Assess the morphology of the red blood cells.
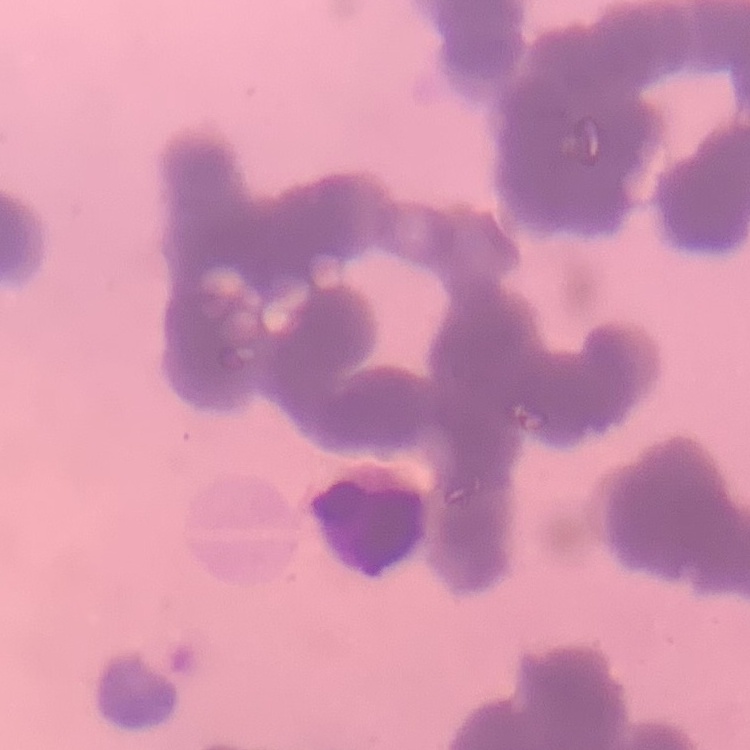
Rouleaux formation.

Square crop of a larger photomicrograph. Thin blood film. Field's or Giemsa stain.